Identify the preparation type.
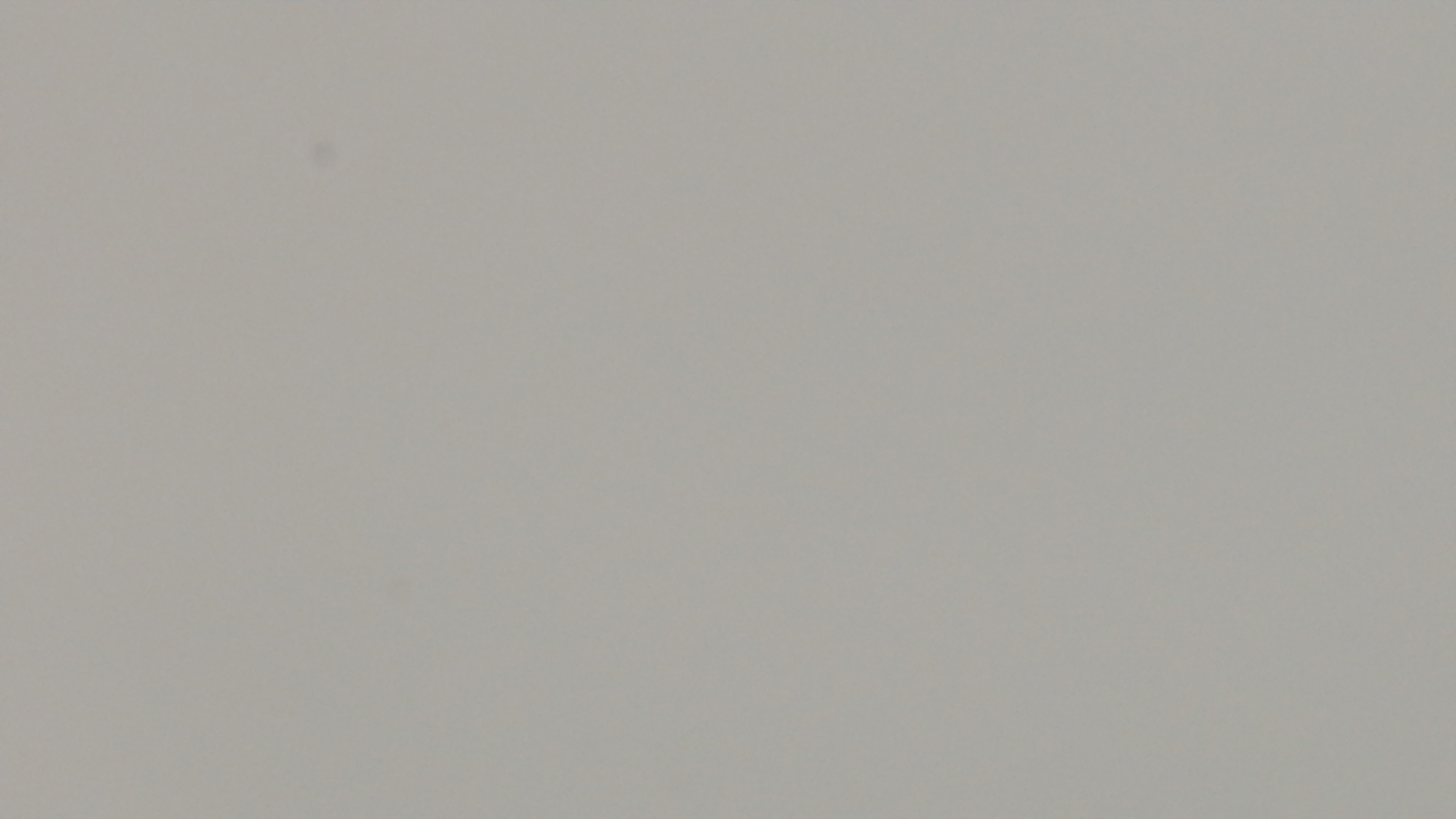

A thin smear.

Summary:
  - Capture: mounted 4K digital camera
  - Malaria status: positive
  - Modality: light microscopy
  - Field of view: one from the slide
  - Objective: 100x oil immersion
  - Stain: Giemsa